Assess the morphology of the red blood cells.
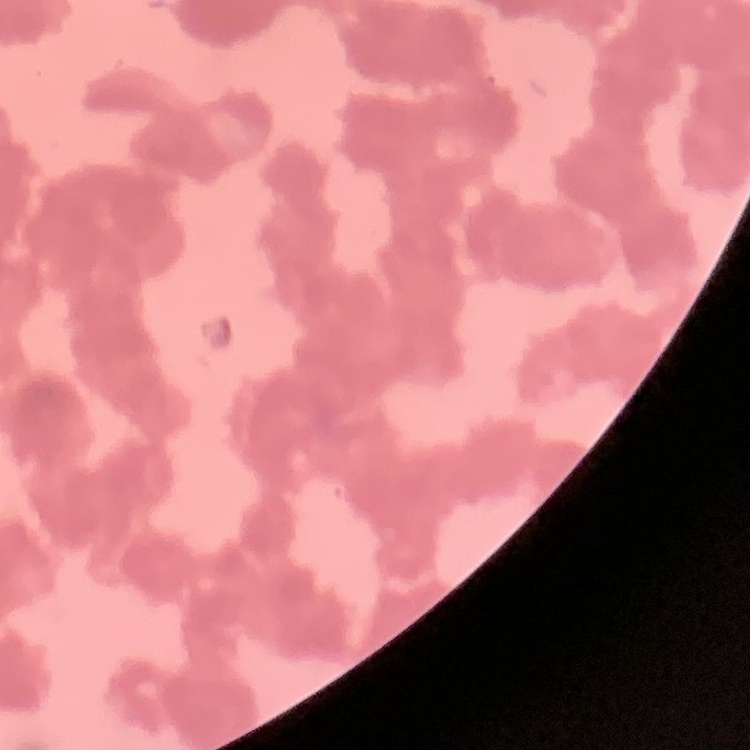

Rouleaux formation.

stain = Field's or Giemsa
image type = one tile cut from a larger photomicrograph
preparation = thin peripheral smear